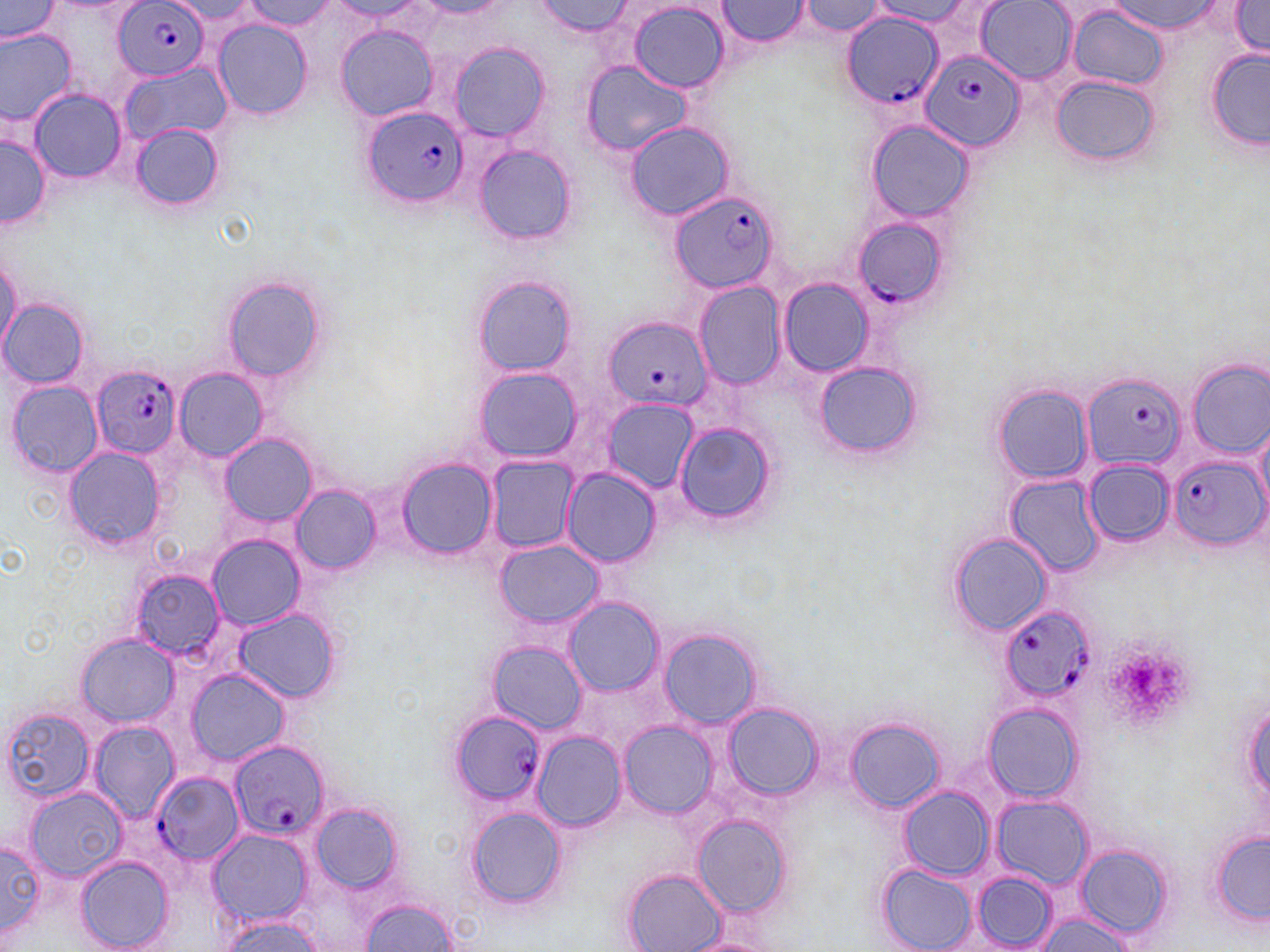
Summary:
  - Coordinate format: approximate bounding boxes as named x1/y1/x2/y2 corners in pixels
  - Platelet locations: (x1=1106, y1=637, x2=1193, y2=729)
  - Uninfected red blood cell locations: (x1=0, y1=0, x2=65, y2=46), (x1=1107, y1=0, x2=1221, y2=34), (x1=168, y1=1, x2=264, y2=29), (x1=241, y1=1, x2=338, y2=31), (x1=333, y1=1, x2=422, y2=18), (x1=536, y1=1, x2=635, y2=37), (x1=714, y1=1, x2=812, y2=47), (x1=976, y1=1, x2=1073, y2=83), (x1=1228, y1=1, x2=1270, y2=58), (x1=628, y1=2, x2=730, y2=92), (x1=795, y1=2, x2=889, y2=36), (x1=867, y1=2, x2=975, y2=25), (x1=1068, y1=6, x2=1169, y2=90), (x1=213, y1=18, x2=313, y2=119), (x1=335, y1=25, x2=438, y2=120), (x1=0, y1=28, x2=76, y2=123), (x1=448, y1=44, x2=550, y2=141), (x1=1205, y1=47, x2=1268, y2=151), (x1=581, y1=61, x2=692, y2=157), (x1=121, y1=62, x2=231, y2=146), (x1=1051, y1=75, x2=1159, y2=168), (x1=28, y1=89, x2=127, y2=182), (x1=624, y1=121, x2=734, y2=221), (x1=867, y1=121, x2=974, y2=220), (x1=130, y1=124, x2=223, y2=209), (x1=0, y1=136, x2=50, y2=228), (x1=474, y1=145, x2=577, y2=243), (x1=1, y1=257, x2=21, y2=351), (x1=221, y1=275, x2=326, y2=383), (x1=473, y1=276, x2=578, y2=374), (x1=778, y1=280, x2=873, y2=375), (x1=693, y1=283, x2=785, y2=390), (x1=0, y1=300, x2=90, y2=388), (x1=1186, y1=359, x2=1270, y2=459), (x1=813, y1=361, x2=923, y2=460), (x1=473, y1=366, x2=583, y2=462), (x1=175, y1=367, x2=267, y2=461), (x1=6, y1=379, x2=103, y2=479), (x1=993, y1=384, x2=1093, y2=484), (x1=602, y1=398, x2=697, y2=494), (x1=1252, y1=418, x2=1270, y2=516), (x1=674, y1=422, x2=775, y2=525), (x1=219, y1=434, x2=317, y2=526), (x1=63, y1=447, x2=166, y2=549), (x1=487, y1=457, x2=578, y2=551), (x1=398, y1=459, x2=497, y2=558), (x1=1082, y1=460, x2=1174, y2=546), (x1=562, y1=468, x2=660, y2=566), (x1=1005, y1=475, x2=1105, y2=578), (x1=292, y1=486, x2=380, y2=574), (x1=948, y1=532, x2=1052, y2=637), (x1=208, y1=534, x2=305, y2=629), (x1=494, y1=540, x2=605, y2=628), (x1=126, y1=565, x2=230, y2=665), (x1=563, y1=598, x2=662, y2=695), (x1=232, y1=609, x2=341, y2=702), (x1=660, y1=628, x2=761, y2=730), (x1=77, y1=634, x2=177, y2=725), (x1=489, y1=641, x2=586, y2=735), (x1=186, y1=669, x2=290, y2=765), (x1=1241, y1=697, x2=1270, y2=807), (x1=725, y1=703, x2=821, y2=799), (x1=983, y1=704, x2=1083, y2=801), (x1=3, y1=709, x2=95, y2=801), (x1=846, y1=719, x2=944, y2=812), (x1=88, y1=721, x2=180, y2=821), (x1=619, y1=722, x2=717, y2=818), (x1=534, y1=731, x2=624, y2=831), (x1=899, y1=786, x2=994, y2=880), (x1=21, y1=788, x2=128, y2=880), (x1=991, y1=795, x2=1093, y2=890), (x1=308, y1=801, x2=404, y2=895), (x1=465, y1=807, x2=567, y2=911), (x1=693, y1=817, x2=792, y2=918), (x1=207, y1=829, x2=313, y2=926), (x1=1211, y1=830, x2=1270, y2=925), (x1=0, y1=839, x2=46, y2=943), (x1=1075, y1=843, x2=1174, y2=939), (x1=74, y1=854, x2=176, y2=952), (x1=878, y1=863, x2=977, y2=952), (x1=623, y1=869, x2=726, y2=952), (x1=969, y1=873, x2=1059, y2=949), (x1=356, y1=898, x2=458, y2=951), (x1=1037, y1=911, x2=1135, y2=952), (x1=214, y1=915, x2=326, y2=952), (x1=680, y1=937, x2=780, y2=952)
  - Plasmodium falciparum-infected red blood cell locations: (x1=113, y1=1, x2=209, y2=81), (x1=842, y1=13, x2=945, y2=110), (x1=921, y1=49, x2=1027, y2=152), (x1=366, y1=108, x2=468, y2=207), (x1=667, y1=189, x2=779, y2=293), (x1=851, y1=215, x2=948, y2=309), (x1=603, y1=316, x2=712, y2=411), (x1=92, y1=366, x2=181, y2=459), (x1=1084, y1=371, x2=1184, y2=471), (x1=1169, y1=456, x2=1265, y2=548), (x1=998, y1=604, x2=1095, y2=700), (x1=448, y1=712, x2=545, y2=803), (x1=228, y1=740, x2=329, y2=842), (x1=153, y1=771, x2=243, y2=865)
  - Slide-level diagnosis: Plasmodium falciparum
  - Image size: 1270×952 pixels
  - Magnification: 1000x
  - Modality: light microscopy
  - Field of view: one of a larger specimen
  - Preparation: thin blood film
  - Stain: May-Grünwald-Giemsa